Locate and identify every blood parasite.
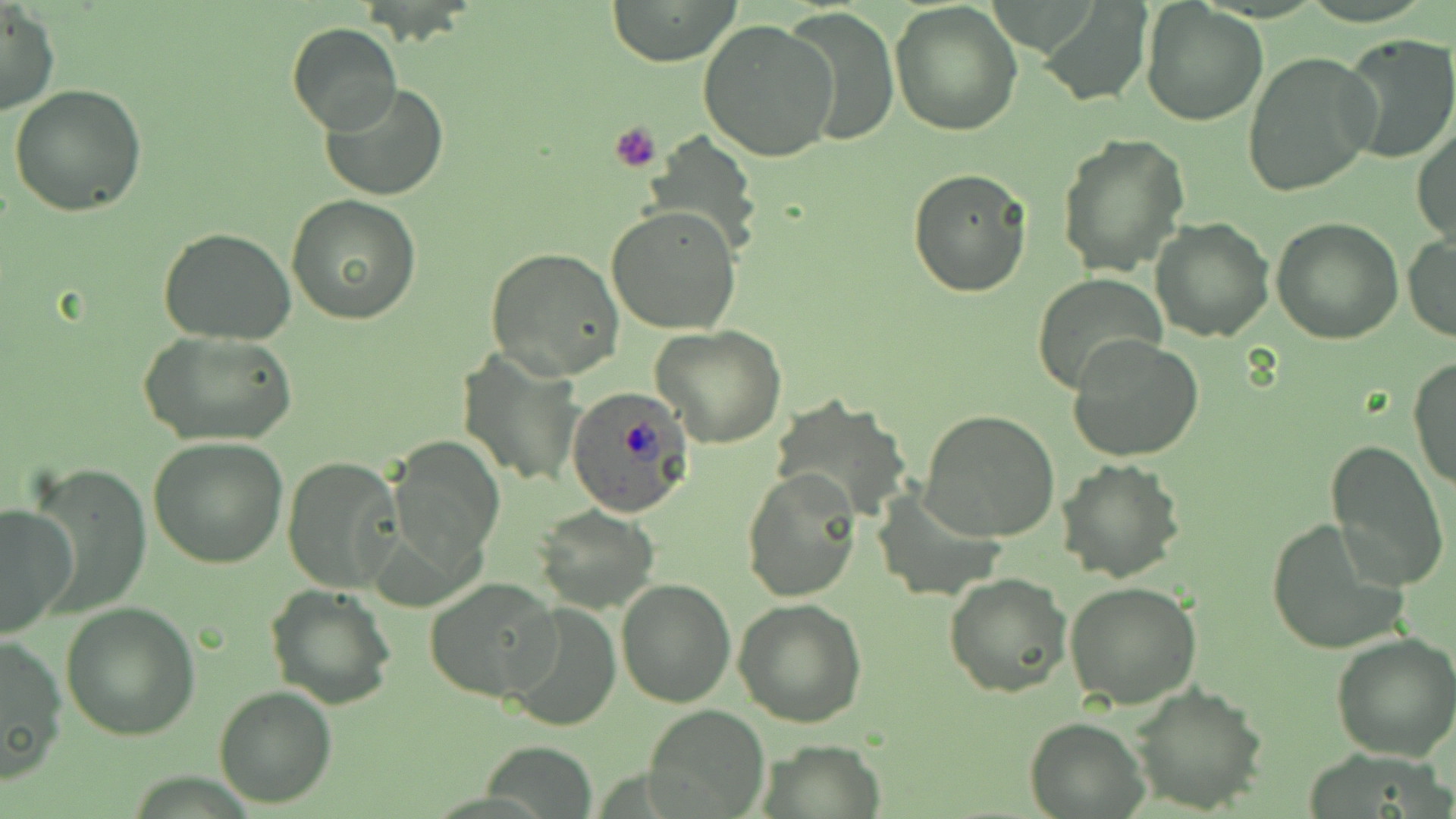
Approximate bounding boxes as (x1, y1, x2, y2) in pixels.
Plasmodium ovale-infected red blood cells: (563, 386, 692, 516).
No Plasmodium falciparum, Plasmodium malariae, Plasmodium vivax, Babesia divergens, or Trypanosoma brucei observed.

slide-level diagnosis = Plasmodium ovale
modality = optical microscopy
field of view = one of a larger specimen
magnification = 1000x
uninfected red blood cell locations = approximate bounding boxes as (x1, y1, x2, y2) in pixels: (606, 0, 742, 66), (889, 2, 1024, 137), (1038, 2, 1153, 107), (2, 3, 59, 117), (1141, 3, 1268, 126), (784, 8, 898, 146), (698, 19, 838, 163), (285, 22, 403, 135), (1338, 33, 1456, 163), (1242, 52, 1378, 197), (322, 82, 449, 201), (7, 83, 150, 217), (1412, 122, 1456, 250), (641, 132, 763, 258), (1056, 132, 1189, 277), (907, 167, 1034, 297), (286, 193, 421, 325), (606, 206, 741, 336), (1150, 216, 1274, 340), (1270, 216, 1403, 343), (157, 227, 298, 346), (1403, 233, 1456, 342), (485, 246, 625, 379), (1032, 274, 1168, 394), (651, 323, 787, 447), (136, 328, 297, 447), (1067, 336, 1204, 464), (456, 349, 582, 487), (1409, 357, 1456, 492), (773, 397, 913, 520), (919, 409, 1061, 542), (389, 435, 506, 570), (147, 436, 289, 568), (1324, 440, 1451, 590), (282, 456, 403, 592), (1055, 458, 1186, 585), (740, 470, 861, 603), (11, 471, 142, 621), (871, 486, 1005, 602), (0, 503, 76, 637), (534, 505, 661, 614), (1265, 517, 1409, 654), (943, 572, 1074, 699), (424, 576, 561, 703), (616, 579, 735, 708), (1063, 580, 1203, 709), (265, 583, 396, 709), (733, 599, 868, 727), (60, 601, 201, 740), (501, 602, 622, 732), (1331, 629, 1456, 760), (0, 632, 68, 783), (1130, 684, 1267, 815), (214, 685, 339, 807), (645, 705, 770, 815), (1023, 716, 1148, 817), (763, 740, 887, 817), (482, 744, 598, 815)
platelet locations = approximate bounding boxes as (x1, y1, x2, y2) in pixels: (609, 121, 661, 173)
preparation = thin blood film
image size = 1456×819 pixels
stain = May-Grünwald-Giemsa